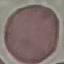
{
  "result": "negative for malaria parasites",
  "image_type": "cell patch, automatically extracted from a larger field of view and resized to 64 × 64 pixels",
  "preparation": "thin smear",
  "stain": "Giemsa",
  "capture": "smartphone through the microscope eyepiece"
}